Assess the morphology of the erythrocytes.
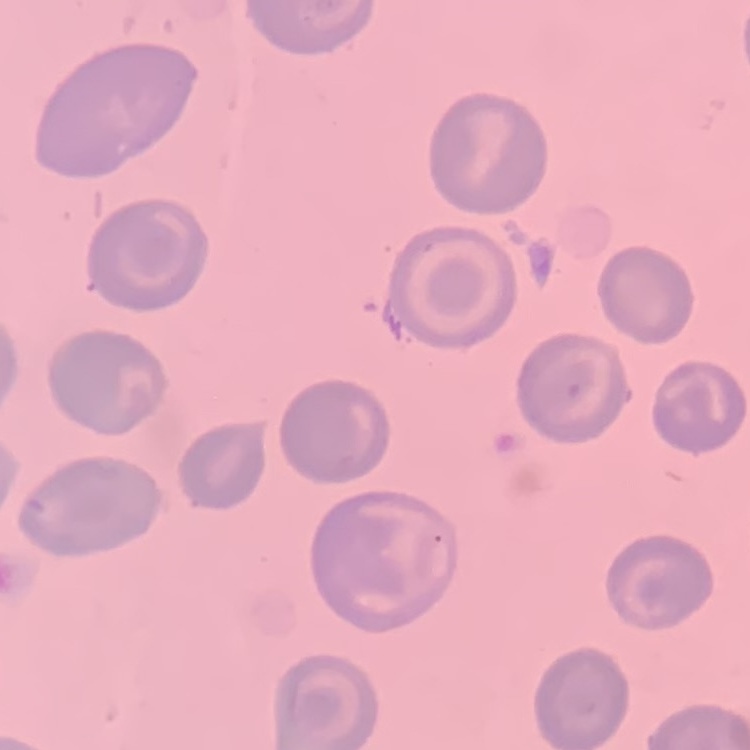

They show no rouleaux formation.

Summary:
  - Preparation: thin blood smear
  - Image type: one tile cut from a larger photomicrograph
  - Stain: Field's or Giemsa